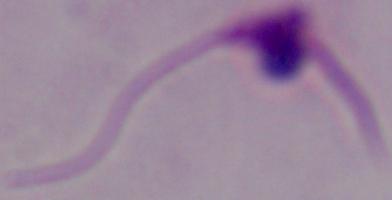

Summary:
  - Identification: Leishmania
  - Magnification: 1000x
  - Modality: photomicrograph